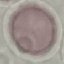

Summary:
  - Malaria status: uninfected
  - Capture: smartphone through the microscope eyepiece
  - Image type: cell patch, automatically extracted from a larger field of view and resized to 64 × 64 pixels
  - Preparation: thin blood smear
  - Stain: Giemsa